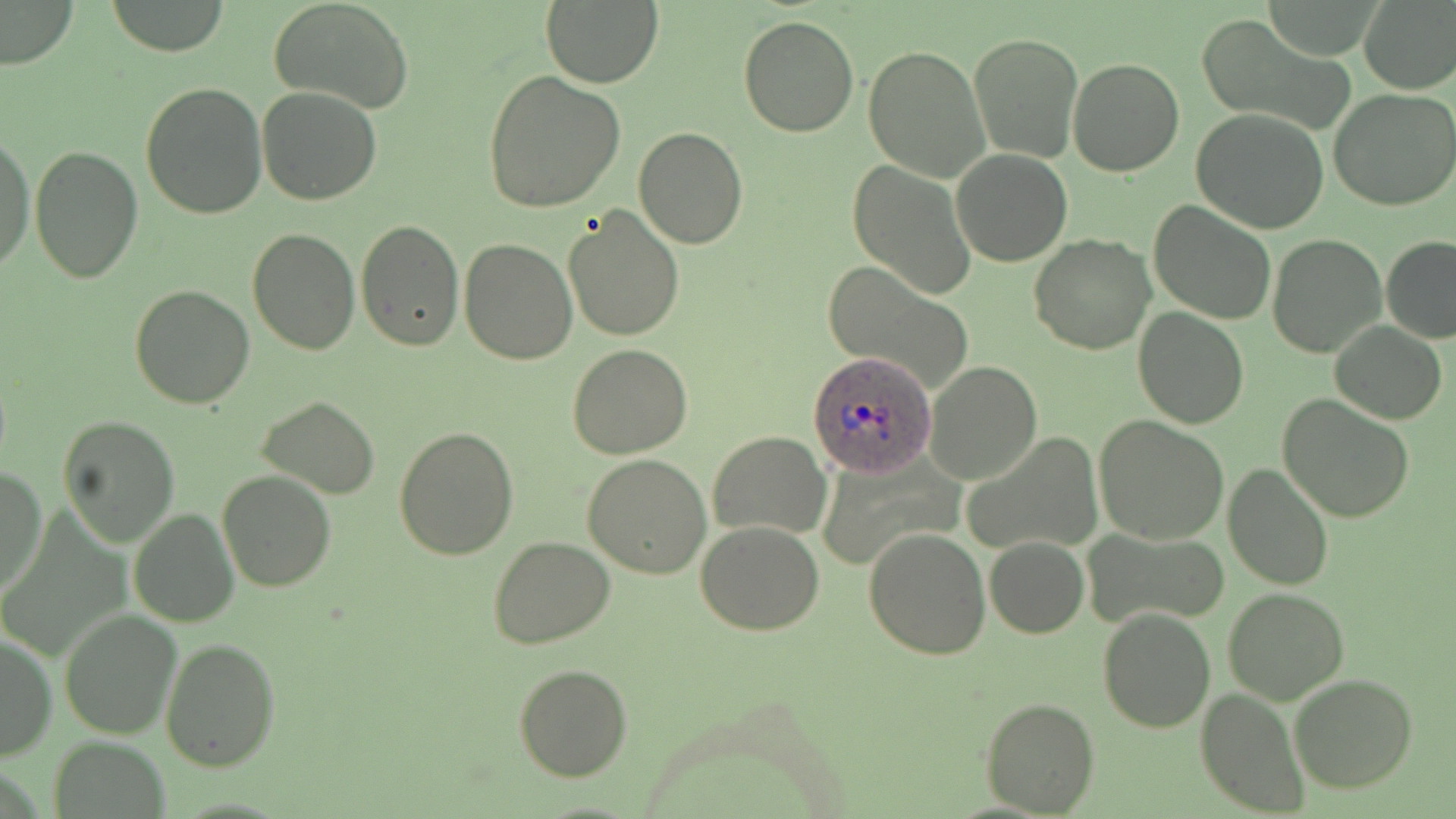
Summary:
  - Coordinate format: approximate bounding boxes as (x1,y1)-(x2,y2) corner pairs in pixels
  - Uninfected red blood cell locations: (1,0)-(77,68), (106,0)-(231,56), (270,0)-(414,114), (540,0)-(664,88), (1356,0)-(1456,94), (736,16)-(858,138), (1197,16)-(1356,136), (968,29)-(1082,163), (862,45)-(990,182), (1065,57)-(1184,177), (483,71)-(627,214), (140,81)-(270,221), (257,86)-(382,204), (1330,89)-(1456,211), (1191,109)-(1329,233), (632,127)-(747,250), (0,134)-(35,272), (28,145)-(143,284), (950,148)-(1072,266), (847,163)-(976,299), (1148,199)-(1276,325), (562,206)-(685,342), (355,220)-(463,352), (247,227)-(360,356), (1266,234)-(1387,359), (1028,235)-(1155,355), (1381,236)-(1456,344), (459,238)-(578,365), (822,263)-(973,393), (129,284)-(254,409), (1133,308)-(1249,429), (1330,323)-(1447,424), (568,343)-(691,458), (923,360)-(1041,485), (1277,395)-(1415,523), (256,396)-(381,498), (56,413)-(181,546), (1093,415)-(1229,545), (394,425)-(521,560), (709,430)-(832,540), (967,432)-(1101,555), (583,452)-(712,578), (1224,460)-(1334,589), (1,468)-(47,598), (216,471)-(339,592), (130,508)-(239,627), (696,520)-(824,634), (864,527)-(991,660), (1081,527)-(1228,632), (487,534)-(616,649), (983,535)-(1090,639), (1223,587)-(1349,704), (1097,607)-(1216,733), (59,611)-(181,739), (0,629)-(56,762), (159,638)-(281,773), (515,664)-(632,781), (1290,672)-(1419,793), (1197,688)-(1310,817), (980,697)-(1100,817), (51,739)-(170,817)
  - Plasmodium ovale-infected red blood cell locations: (808,350)-(939,478)
  - Slide-level diagnosis: Plasmodium ovale
  - Image size: 1456×819 pixels
  - Stain: May-Grünwald-Giemsa
  - Preparation: thin blood film
  - Magnification: 1000x
  - Modality: optical microscopy
  - Field of view: single